State which parasite is depicted.
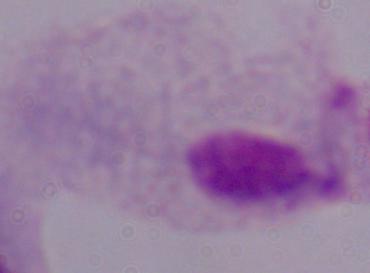
This is a trichomonad.

Captured at 1000x magnification. Micrograph.